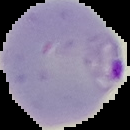

From a thin blood smear. Result: Plasmodium parasites detected. Cell region segmented out of the field of view; the surrounding area is masked to black. Image is 130×130 pixels.